Assess this cell for malaria.
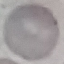
It is uninfected.

Cell patch, automatically extracted from a larger field of view and resized to 64 × 64 pixels. Thin smear of blood. Giemsa-stained preparation. Photographed with a smartphone camera at the microscope eyepiece.